Locate every blood parasite and identify its species.
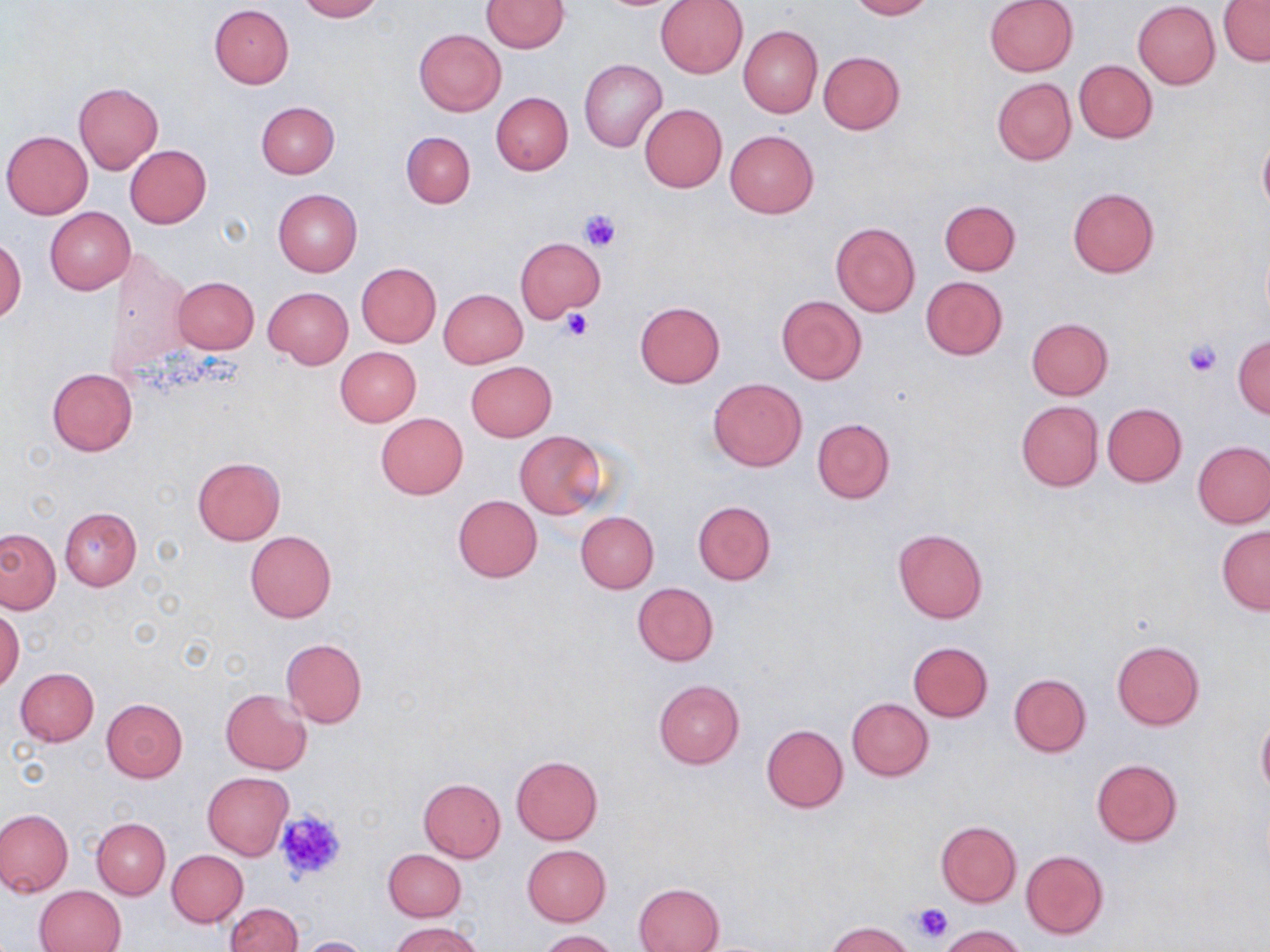
No blood parasites seen.

slide-level diagnosis = no evidence of blood parasites
modality = light microscopy
field of view = one of a larger specimen
magnification = 1000x
preparation = thin blood smear
uninfected red blood cell locations = approximate bounding boxes as [x1, y1, x2, y2] in pixels: [297, 0, 383, 21], [482, 0, 570, 53], [656, 0, 748, 78], [849, 0, 933, 19], [984, 0, 1079, 76], [1133, 1, 1220, 88], [1219, 1, 1270, 66], [209, 4, 294, 88], [738, 25, 823, 118], [413, 28, 506, 116], [819, 51, 904, 134], [579, 59, 667, 153], [1074, 60, 1157, 143], [992, 78, 1076, 166], [73, 82, 163, 174], [491, 92, 573, 175], [256, 101, 340, 178], [639, 104, 727, 193], [2, 130, 93, 218], [724, 130, 819, 219], [402, 131, 476, 208], [1257, 131, 1270, 219], [124, 145, 211, 228], [1068, 188, 1159, 278], [273, 189, 362, 278], [940, 199, 1020, 276], [45, 207, 135, 294], [830, 222, 920, 317], [0, 234, 26, 324], [515, 237, 606, 325], [106, 249, 191, 377], [356, 262, 441, 347], [172, 276, 259, 353], [921, 276, 1008, 359], [264, 287, 353, 368], [438, 288, 527, 368], [776, 295, 868, 385], [633, 302, 725, 388], [1026, 318, 1113, 399], [1233, 333, 1270, 418], [335, 346, 421, 427], [465, 361, 557, 441], [46, 367, 138, 455], [708, 377, 808, 472], [1016, 400, 1103, 491], [1102, 403, 1187, 486], [376, 412, 468, 499], [812, 419, 895, 504], [514, 431, 609, 518], [1193, 440, 1270, 528], [192, 457, 286, 546], [452, 495, 543, 582], [693, 501, 775, 585], [59, 507, 141, 591], [575, 511, 659, 593], [1216, 526, 1270, 614], [0, 528, 60, 614], [893, 528, 987, 624], [245, 530, 336, 623], [633, 582, 719, 666], [0, 608, 24, 692], [280, 637, 367, 727], [1112, 640, 1204, 729], [908, 641, 993, 722], [15, 668, 99, 746], [1009, 673, 1091, 757], [654, 680, 745, 769], [220, 689, 312, 773], [101, 698, 189, 783], [846, 698, 934, 781], [1256, 717, 1270, 796], [762, 723, 848, 812], [511, 755, 604, 844], [1090, 758, 1184, 848], [202, 772, 294, 860], [418, 778, 507, 862], [0, 808, 73, 897], [92, 817, 170, 900], [935, 821, 1022, 906], [522, 844, 611, 925], [168, 849, 248, 926], [383, 849, 465, 920], [1020, 849, 1110, 939], [633, 882, 724, 951], [35, 884, 127, 952], [226, 903, 302, 952], [390, 921, 483, 952], [824, 921, 916, 952], [939, 925, 1029, 952], [537, 930, 619, 952], [296, 936, 374, 952]
stain = May-Grünwald-Giemsa
image size = 1270×952 pixels
platelet locations = approximate bounding boxes as [x1, y1, x2, y2] in pixels: [578, 208, 621, 252], [560, 311, 593, 340], [1183, 340, 1223, 377], [272, 809, 347, 884], [911, 904, 954, 945]